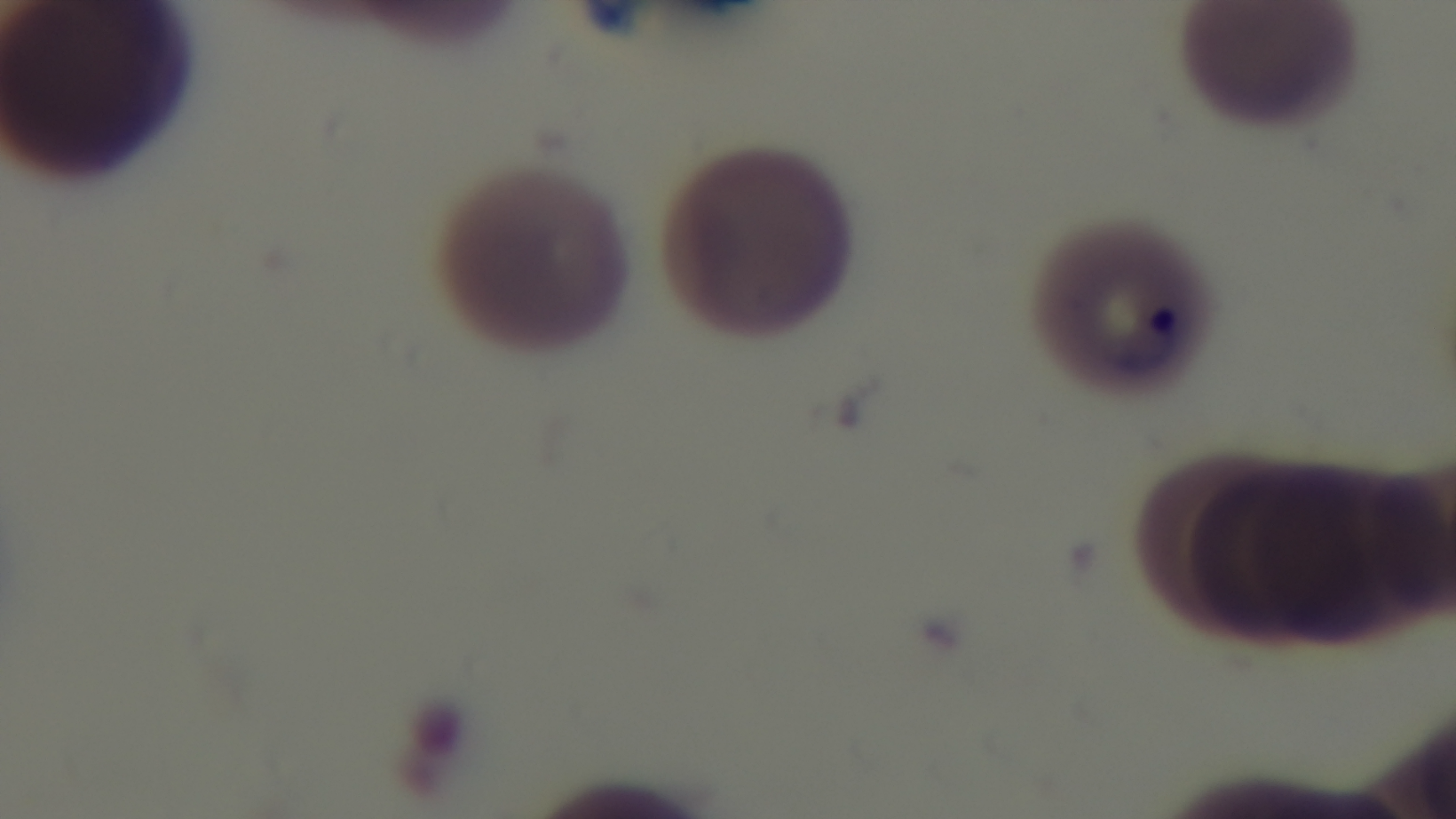
Oil-immersion objective, 100x. Mounted 4K digital camera. Light microscopy. Single field of view. Preparation: thin. Giemsa stain. Malaria status: infected.